Report the malaria status of this cell.
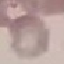

Uninfected.

Summary:
  - Stain: Giemsa
  - Capture: smartphone through the microscope eyepiece
  - Image type: automatically extracted cell patch, resized to 64 × 64 pixels
  - Preparation: thin blood film